Outline each blood parasite and name the species.
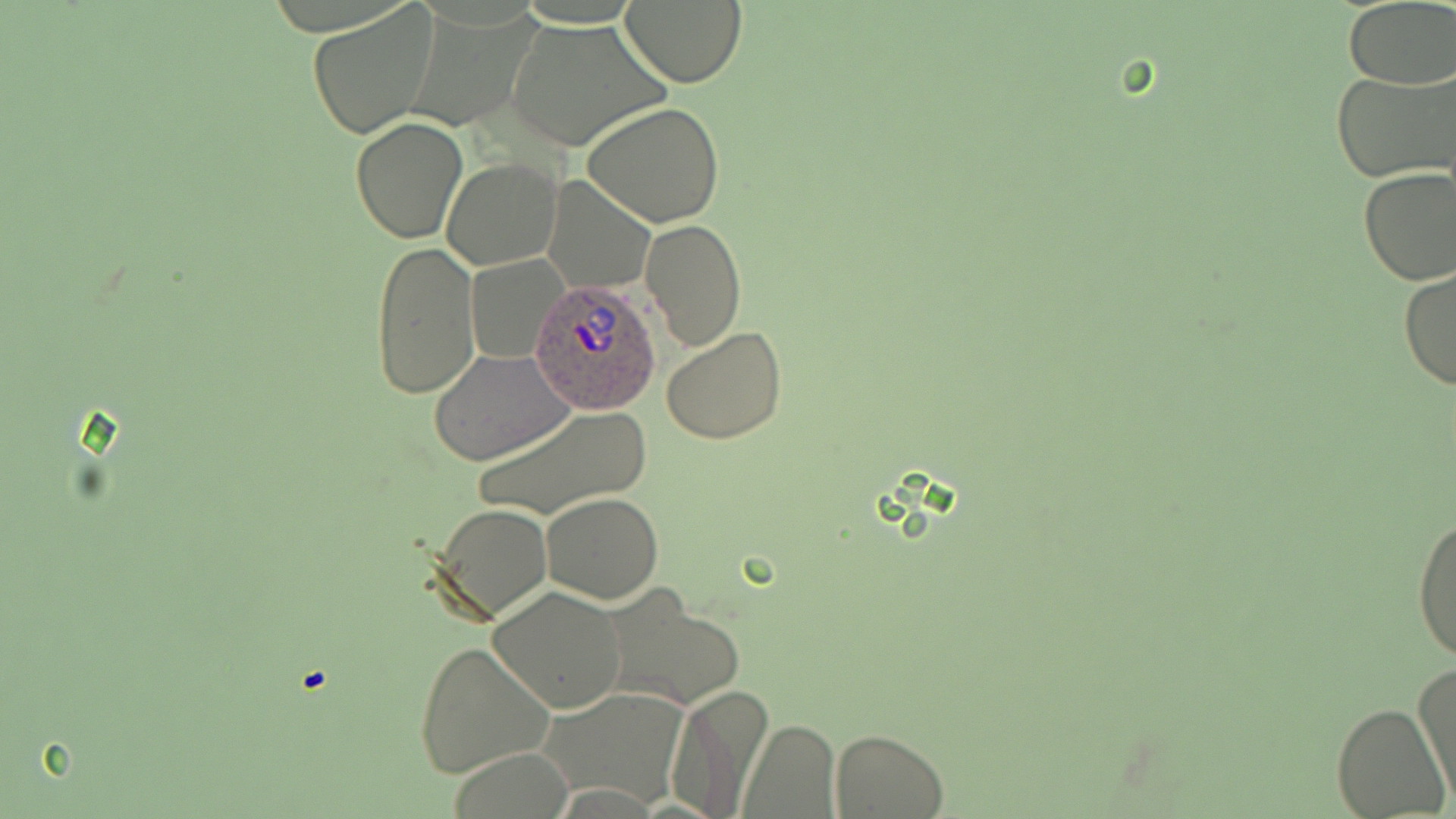

Approximate bounding boxes as named x1/y1/x2/y2 corners in pixels.
Plasmodium ovale-infected red blood cells: (x1=531, y1=279, x2=661, y2=415).
No Plasmodium falciparum, Plasmodium malariae, Plasmodium vivax, Babesia divergens, or Trypanosoma brucei observed.

slide-level diagnosis = Plasmodium ovale
preparation = thin blood smear
modality = optical microscopy
uninfected red blood cell locations = approximate bounding boxes as named x1/y1/x2/y2 corners in pixels: (x1=619, y1=0, x2=746, y2=86), (x1=308, y1=2, x2=440, y2=140), (x1=1343, y1=3, x2=1456, y2=87), (x1=506, y1=20, x2=666, y2=153), (x1=1332, y1=67, x2=1456, y2=185), (x1=582, y1=100, x2=727, y2=229), (x1=350, y1=117, x2=467, y2=243), (x1=443, y1=159, x2=562, y2=270), (x1=1357, y1=167, x2=1456, y2=286), (x1=542, y1=175, x2=655, y2=292), (x1=639, y1=218, x2=746, y2=352), (x1=370, y1=240, x2=479, y2=400), (x1=468, y1=253, x2=564, y2=364), (x1=1397, y1=266, x2=1455, y2=391), (x1=660, y1=324, x2=786, y2=445), (x1=429, y1=348, x2=574, y2=466), (x1=471, y1=403, x2=651, y2=522), (x1=540, y1=493, x2=665, y2=603), (x1=431, y1=503, x2=554, y2=624), (x1=1411, y1=508, x2=1456, y2=666), (x1=487, y1=586, x2=627, y2=714), (x1=602, y1=587, x2=744, y2=713), (x1=412, y1=640, x2=555, y2=779), (x1=1413, y1=663, x2=1455, y2=802), (x1=662, y1=685, x2=771, y2=817), (x1=539, y1=688, x2=687, y2=807), (x1=1333, y1=702, x2=1450, y2=818), (x1=739, y1=721, x2=839, y2=816), (x1=830, y1=728, x2=948, y2=817)
magnification = 1000x
image size = 1456×819 pixels
stain = May-Grünwald-Giemsa
field of view = one of a larger specimen